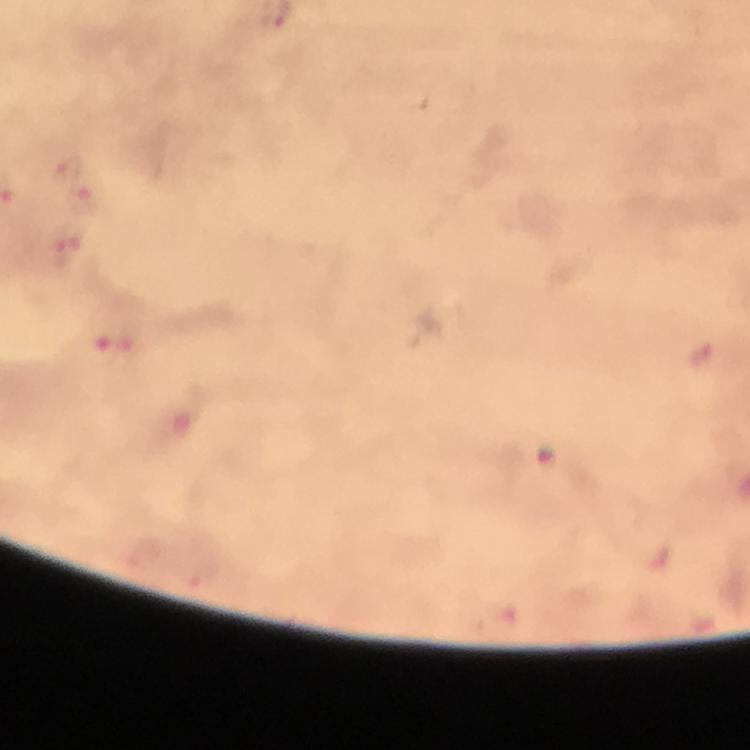
stain = Giemsa
image size = 750×750 pixels
cropped from = a single field of view
Plasmodium parasite locations = approximate object centers, in pixels from the top-left corner: (x=68, y=168), (x=85, y=199), (x=69, y=249), (x=704, y=354)
preparation = thick blood film
immersion oil = applied
capture = smartphone photograph through a microscope
context = from a malaria diagnostic workup
magnification = 100x